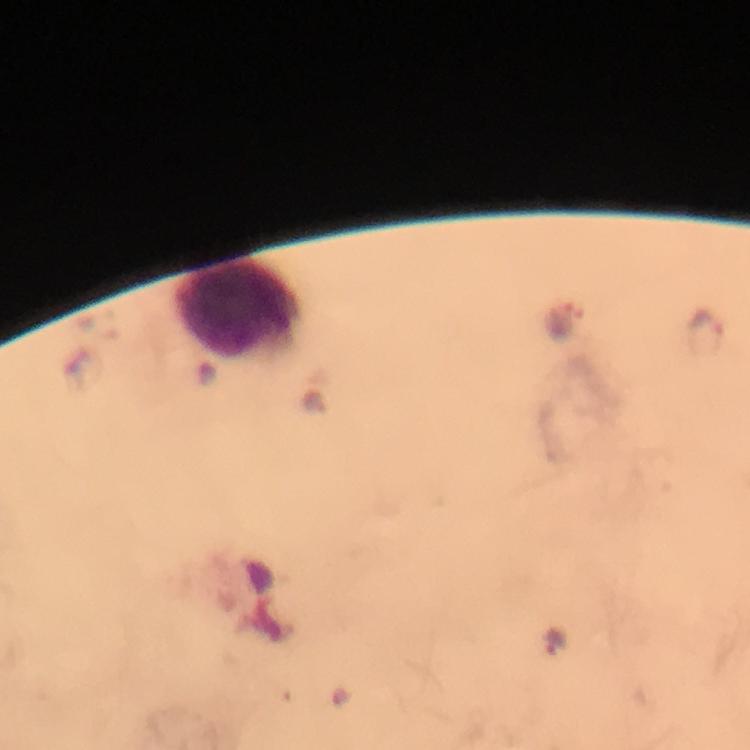 Approximate object centers, in pixels from the top-left corner. Plasmodium parasite locations: (x=705, y=331), (x=556, y=641). Leukocyte locations: (x=236, y=309). Immersion oil was used. From a diagnostic examination for malaria. Thick blood smear. Image is 750×750 pixels. Giemsa stain. At 100x magnification. A crop from one field of view. Smartphone photograph taken through a microscope.